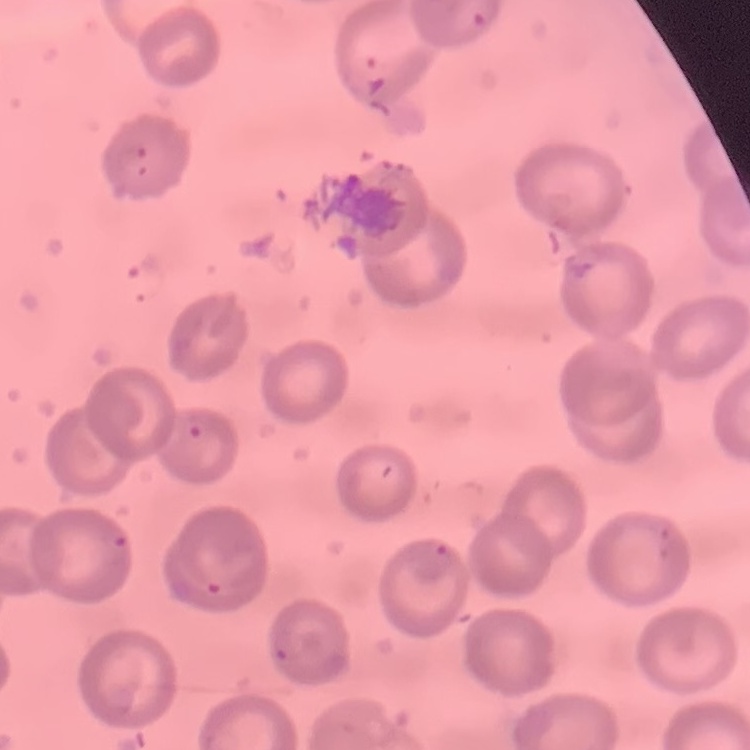
Summary:
  - Erythrocyte morphology: no rouleaux formation
  - Image type: one tile cut from a larger photomicrograph
  - Stain: Field's or Giemsa
  - Preparation: thin blood film